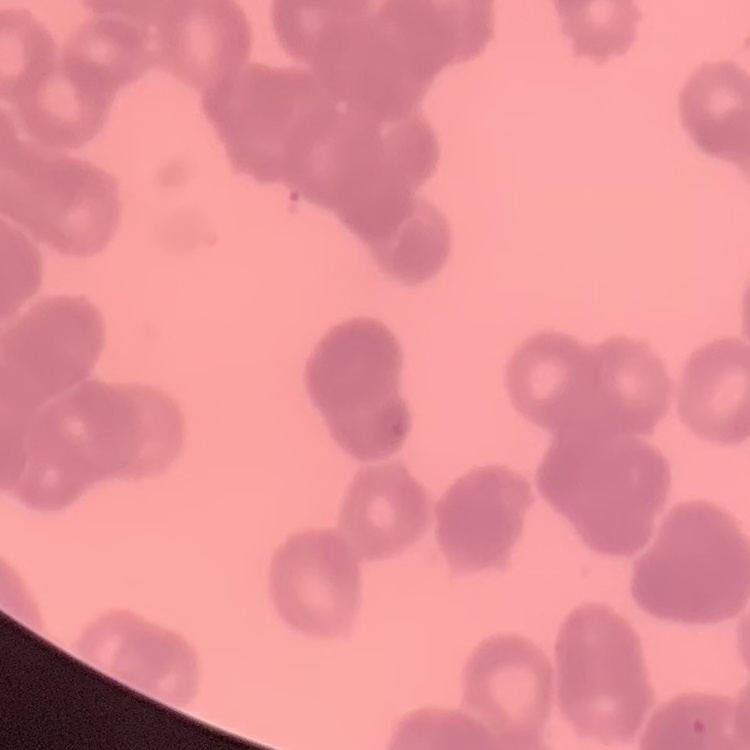

Summary:
  - Erythrocyte morphology: rouleaux formation
  - Preparation: thin blood film
  - Stain: Field's or Giemsa
  - Image type: one tile cut from a larger photomicrograph